Assess this cell for malaria.
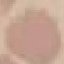

Uninfected.

Summary:
  - Stain: Giemsa
  - Capture: smartphone camera at the microscope eyepiece
  - Image type: automatically extracted cell patch, resized to 64 × 64 pixels
  - Preparation: thin blood smear